Classify this cell by malaria status.
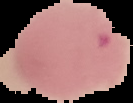
Parasitized.

Summary:
  - Preparation: thin blood smear
  - Image type: cell region segmented out of the field of view; surrounding area masked to black
  - Image size: 133×103 pixels